Classify this cell by malaria status.
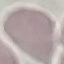

Uninfected.

Cell patch, automatically extracted from a larger field of view and resized to 64 × 64 pixels. Photographed with a smartphone camera at the microscope eyepiece. Thin blood smear. Giemsa stain.